Assess the morphology of the erythrocytes.
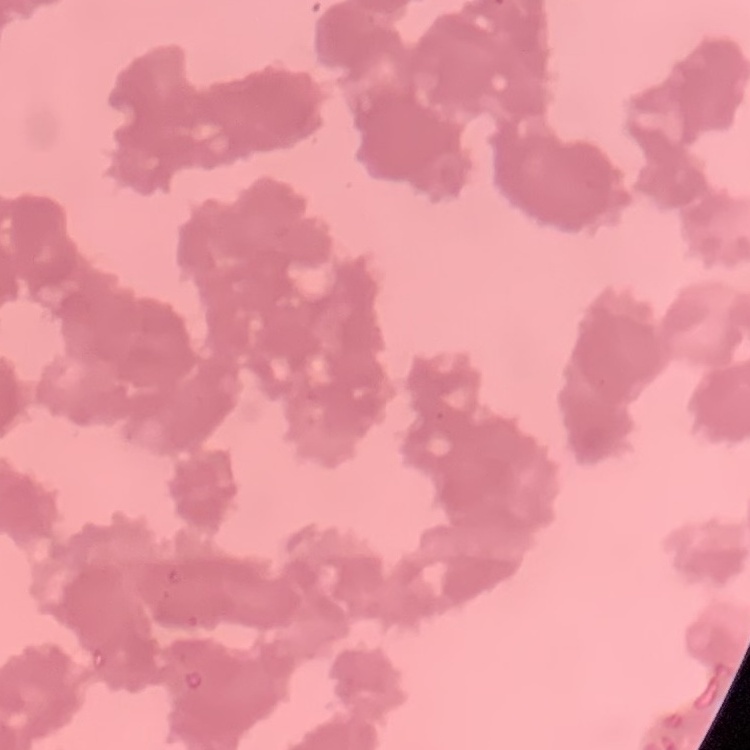

Rouleaux formation.

Square crop of a larger photomicrograph. Thin peripheral smear. Stained with either Field's or Giemsa.